Classify this cell by malaria status.
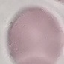

Uninfected.

Summary:
  - Stain: Giemsa
  - Preparation: thin blood smear
  - Capture: smartphone camera at the microscope eyepiece
  - Image type: automatically extracted cell patch, resized to 64 × 64 pixels